Assess this cell for malaria.
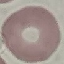
It is uninfected.

Summary:
  - Preparation: thin blood film
  - Image type: cell patch, automatically extracted from a larger field of view and resized to 64 × 64 pixels
  - Stain: Giemsa
  - Capture: smartphone through the microscope eyepiece